Report the malaria status of this cell.
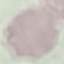

Uninfected.

Summary:
  - Capture: smartphone camera at the microscope eyepiece
  - Image type: cell patch, automatically extracted from a larger field of view and resized to 64 × 64 pixels
  - Preparation: thin blood smear
  - Stain: Giemsa